Identify the parasite.
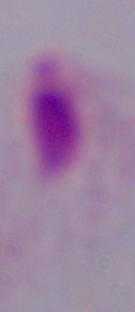
A trichomonad.

Captured at 1000x magnification. Photomicrograph.